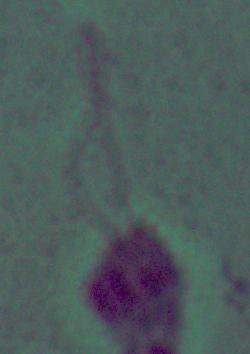
Summary:
  - Modality: micrograph
  - Magnification: 1000x
  - Identification: Leishmania